Assess this cell for malaria.
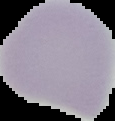
Uninfected.

image size = 115×121 pixels
image type = cell region segmented out of the field of view; surrounding area masked to black
preparation = thin blood smear